Classify this cell by malaria status.
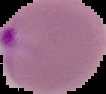

Parasitized.

image_size: 106×94 pixels
image_type: segmented cell region with the area outside set to black
preparation: thin blood film